Locate every P. falciparum parasite and give its life-cycle stage, and locate every leukocyte and any debris.
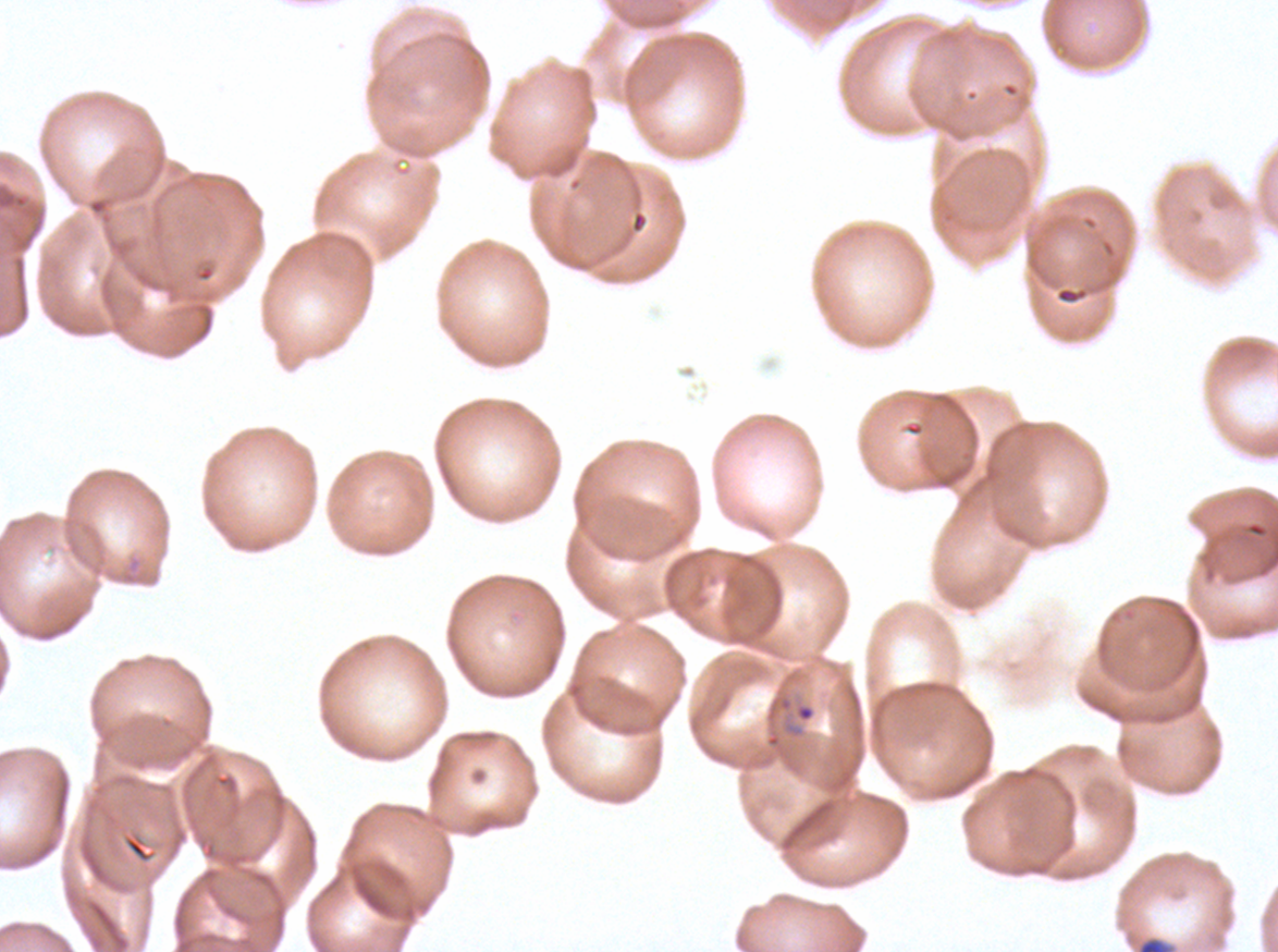
Approximate bounding boxes as (x1, y1, x2, y2) in pixels.
Rings: (796, 704, 815, 722).
Debris: (1137, 936, 1172, 951).
No late-ring/early-trophozoite forms, mid trophozoites, late trophozoites, early schizonts, late schizonts, segmenters, gametocytes, or leukocytes observed.

One sub-image of a larger composite. Giemsa-stained preparation. Image is 1278×952 pixels. Thin blood film. Ex-vivo P. falciparum culture from a patient in The Gambia, grown for 24 to 48 hours.